State which parasite is depicted.
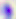
This is Toxoplasma gondii.

modality: photomicrograph
magnification: 400x